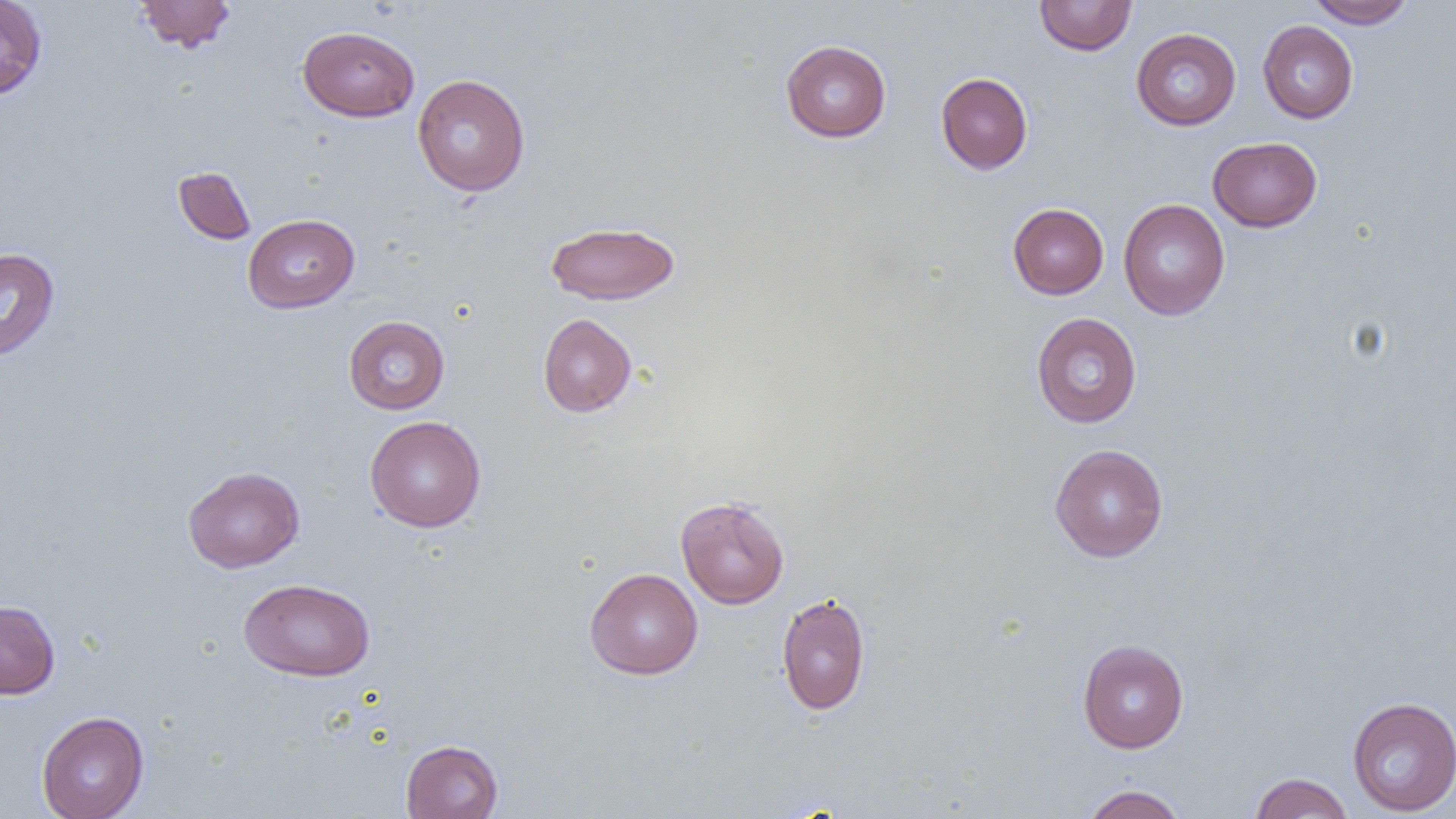
Summary:
  - Coordinate format: approximate bounding boxes as named x1/y1/x2/y2 corners in pixels
  - Uninfected red blood cell locations: (x1=0, y1=0, x2=48, y2=100), (x1=1034, y1=0, x2=1137, y2=56), (x1=1308, y1=0, x2=1416, y2=29), (x1=134, y1=1, x2=236, y2=53), (x1=1257, y1=20, x2=1358, y2=124), (x1=297, y1=25, x2=419, y2=122), (x1=1131, y1=27, x2=1241, y2=130), (x1=780, y1=39, x2=892, y2=142), (x1=935, y1=72, x2=1033, y2=174), (x1=412, y1=74, x2=530, y2=196), (x1=1208, y1=136, x2=1322, y2=232), (x1=173, y1=166, x2=256, y2=245), (x1=1118, y1=198, x2=1230, y2=320), (x1=1007, y1=203, x2=1109, y2=299), (x1=243, y1=214, x2=359, y2=313), (x1=545, y1=220, x2=680, y2=305), (x1=0, y1=248, x2=59, y2=361), (x1=1031, y1=312, x2=1142, y2=428), (x1=537, y1=313, x2=637, y2=417), (x1=343, y1=315, x2=450, y2=414), (x1=365, y1=415, x2=486, y2=532), (x1=1049, y1=443, x2=1168, y2=563), (x1=183, y1=466, x2=305, y2=573), (x1=675, y1=495, x2=789, y2=609), (x1=585, y1=567, x2=703, y2=680), (x1=239, y1=578, x2=375, y2=682), (x1=776, y1=592, x2=871, y2=716), (x1=0, y1=600, x2=60, y2=699), (x1=1077, y1=639, x2=1189, y2=753), (x1=1347, y1=696, x2=1456, y2=816), (x1=36, y1=710, x2=149, y2=819), (x1=401, y1=739, x2=503, y2=818), (x1=1249, y1=772, x2=1354, y2=818), (x1=1081, y1=784, x2=1188, y2=819)
  - Slide-level diagnosis: negative for blood parasites
  - Modality: light microscopy
  - Magnification: 1000x
  - Image size: 1456×819 pixels
  - Preparation: thin blood film
  - Field of view: one of a larger specimen